Name the cell type shown.
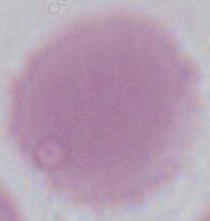

This is an erythrocyte.

magnification = 1000x
modality = micrograph